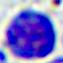
Summary:
  - Modality: photomicrograph
  - Magnification: 400x
  - Identification: white blood cell